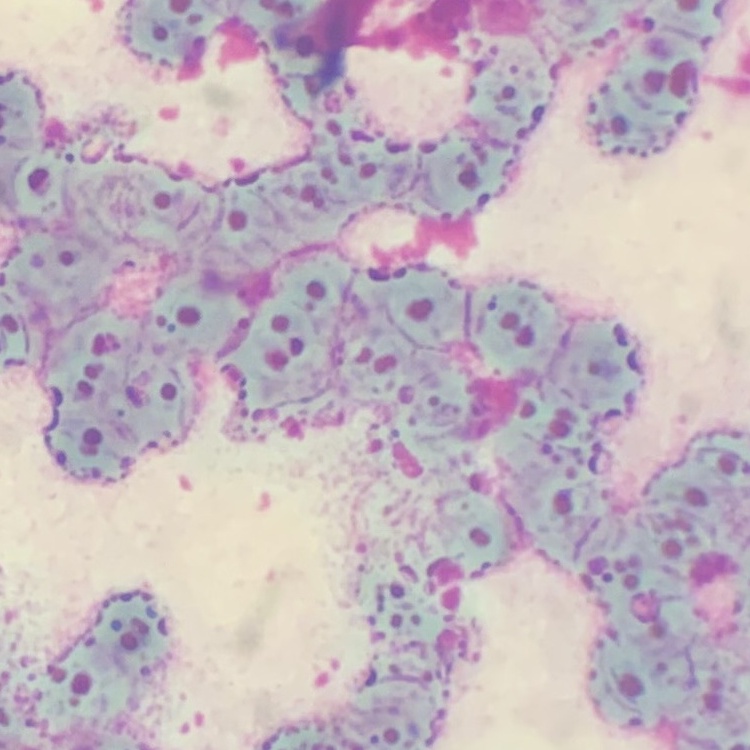

red blood cell morphology = rouleaux formation
image type = square crop of a larger photomicrograph
stain = Field's or Giemsa
preparation = thin peripheral smear